Locate every blood parasite and identify its species.
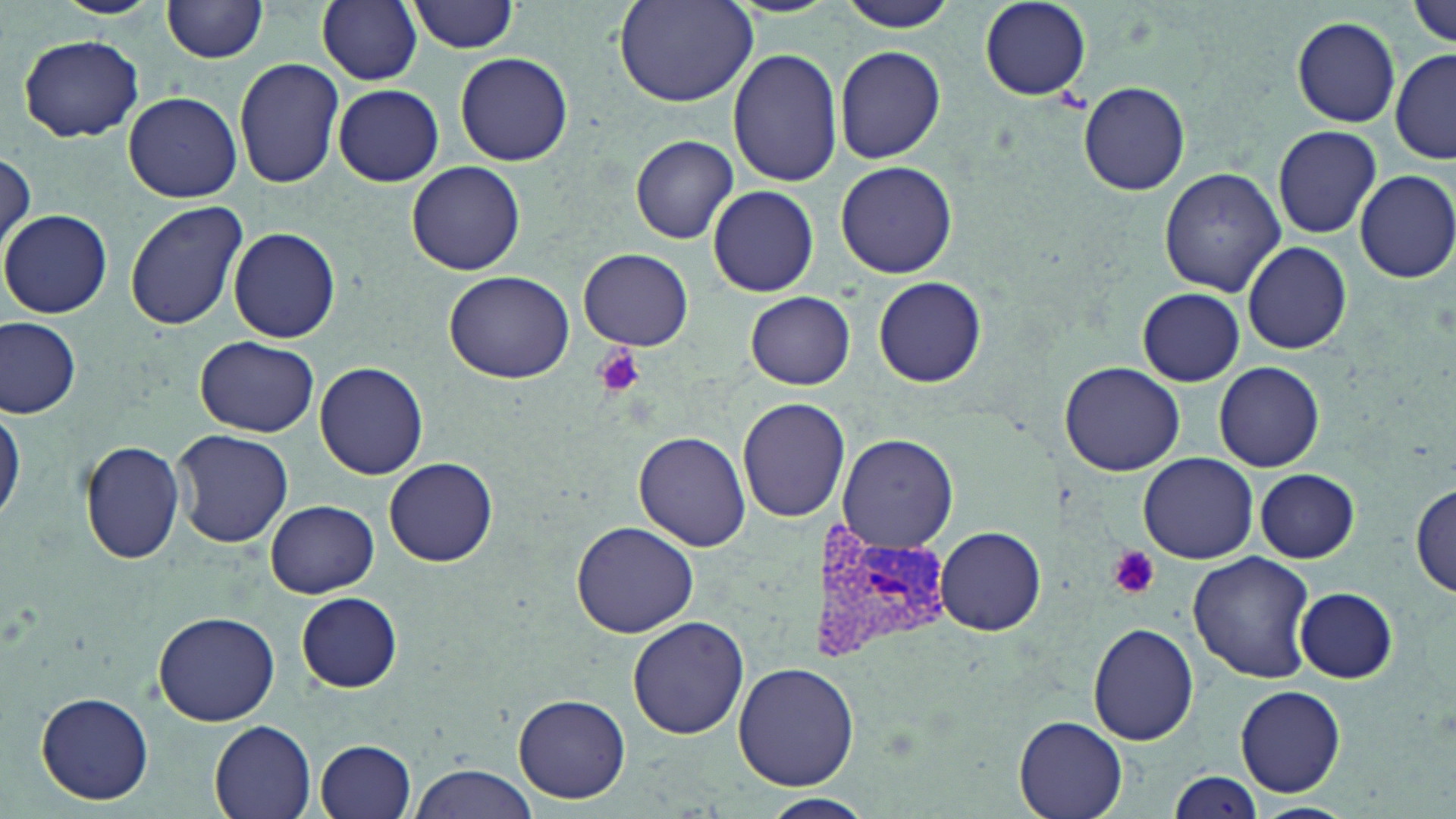

Approximate bounding boxes as (x1, y1, x2, y2) in pixels.
Plasmodium vivax-infected red blood cells: (812, 523, 952, 664).
No Plasmodium falciparum, Plasmodium ovale, Plasmodium malariae, Babesia divergens, or Trypanosoma brucei observed.

Summary:
  - Platelet locations: (595, 347, 645, 399), (1108, 546, 1160, 598)
  - Uninfected red blood cell locations: (317, 0, 422, 86), (407, 0, 521, 53), (610, 0, 759, 108), (833, 0, 960, 32), (161, 1, 271, 64), (978, 1, 1092, 100), (1409, 1, 1455, 49), (1293, 16, 1400, 127), (17, 34, 145, 142), (835, 46, 946, 164), (728, 49, 844, 187), (1391, 50, 1456, 165), (455, 52, 573, 167), (234, 58, 344, 189), (1078, 81, 1190, 196), (333, 85, 444, 186), (124, 91, 242, 202), (1271, 126, 1381, 239), (630, 135, 737, 244), (0, 151, 34, 261), (407, 161, 526, 275), (836, 162, 957, 278), (1159, 168, 1284, 296), (1355, 170, 1456, 283), (708, 184, 820, 296), (123, 199, 248, 330), (1, 210, 112, 319), (227, 227, 339, 344), (1243, 241, 1353, 355), (580, 249, 693, 350), (443, 270, 576, 384), (873, 277, 987, 388), (1137, 288, 1245, 386), (746, 293, 857, 388), (0, 317, 81, 418), (195, 336, 319, 438), (1061, 361, 1185, 475), (1215, 362, 1324, 472), (315, 363, 427, 479), (736, 396, 846, 522), (0, 405, 24, 527), (170, 428, 293, 547), (634, 431, 752, 552), (838, 433, 959, 552), (80, 439, 185, 565), (1139, 452, 1258, 563), (384, 458, 497, 567), (1255, 469, 1360, 563), (1411, 482, 1456, 596), (265, 499, 379, 598), (569, 521, 697, 639), (935, 526, 1046, 635), (1185, 550, 1314, 685), (1294, 587, 1398, 682), (297, 591, 402, 692), (153, 611, 280, 726), (627, 615, 749, 740), (1088, 623, 1199, 746), (733, 661, 859, 790), (1236, 685, 1346, 796), (37, 692, 154, 807), (515, 695, 630, 802), (1012, 716, 1128, 819), (208, 718, 318, 819), (316, 739, 417, 819), (407, 762, 542, 819), (1168, 771, 1263, 817), (759, 793, 875, 819), (1250, 802, 1357, 819)
  - Slide-level diagnosis: Plasmodium vivax
  - Stain: May-Grünwald-Giemsa
  - Image size: 1456×819 pixels
  - Preparation: thin blood smear
  - Modality: light microscopy
  - Field of view: single
  - Magnification: 1000x